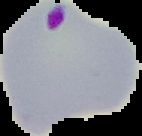
Summary:
  - Image size: 142×136 pixels
  - Preparation: thin blood film
  - Malaria status: parasitized
  - Image type: segmented cell region with the area outside set to black